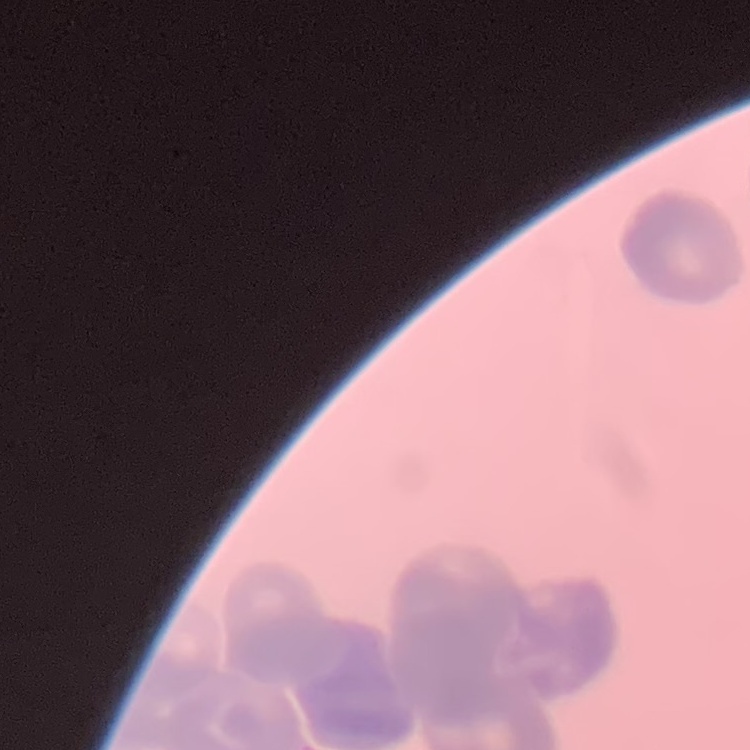

Summary:
  - Erythrocyte morphology: rouleaux formation
  - Preparation: thin blood smear
  - Stain: Field's or Giemsa
  - Image type: square crop of a larger photomicrograph